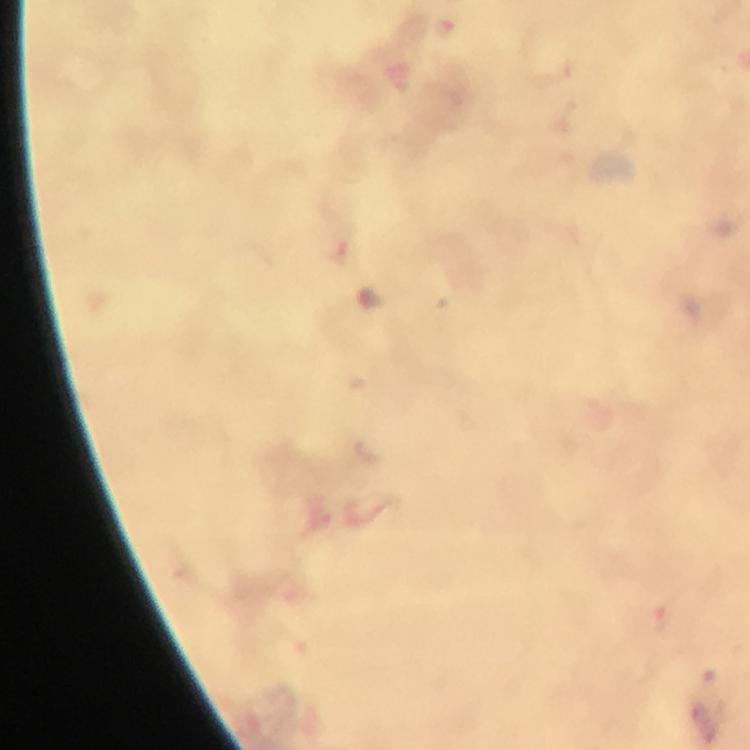

capture = smartphone photograph through a microscope
context = from a malaria diagnostic workup
preparation = thick smear
magnification = 100x
immersion oil = applied
malaria parasite locations = approximate object centers, in pixels from the top-left corner: (x=340, y=253), (x=665, y=619)
image size = 750×750 pixels
cropped from = one field of view
stain = Giemsa